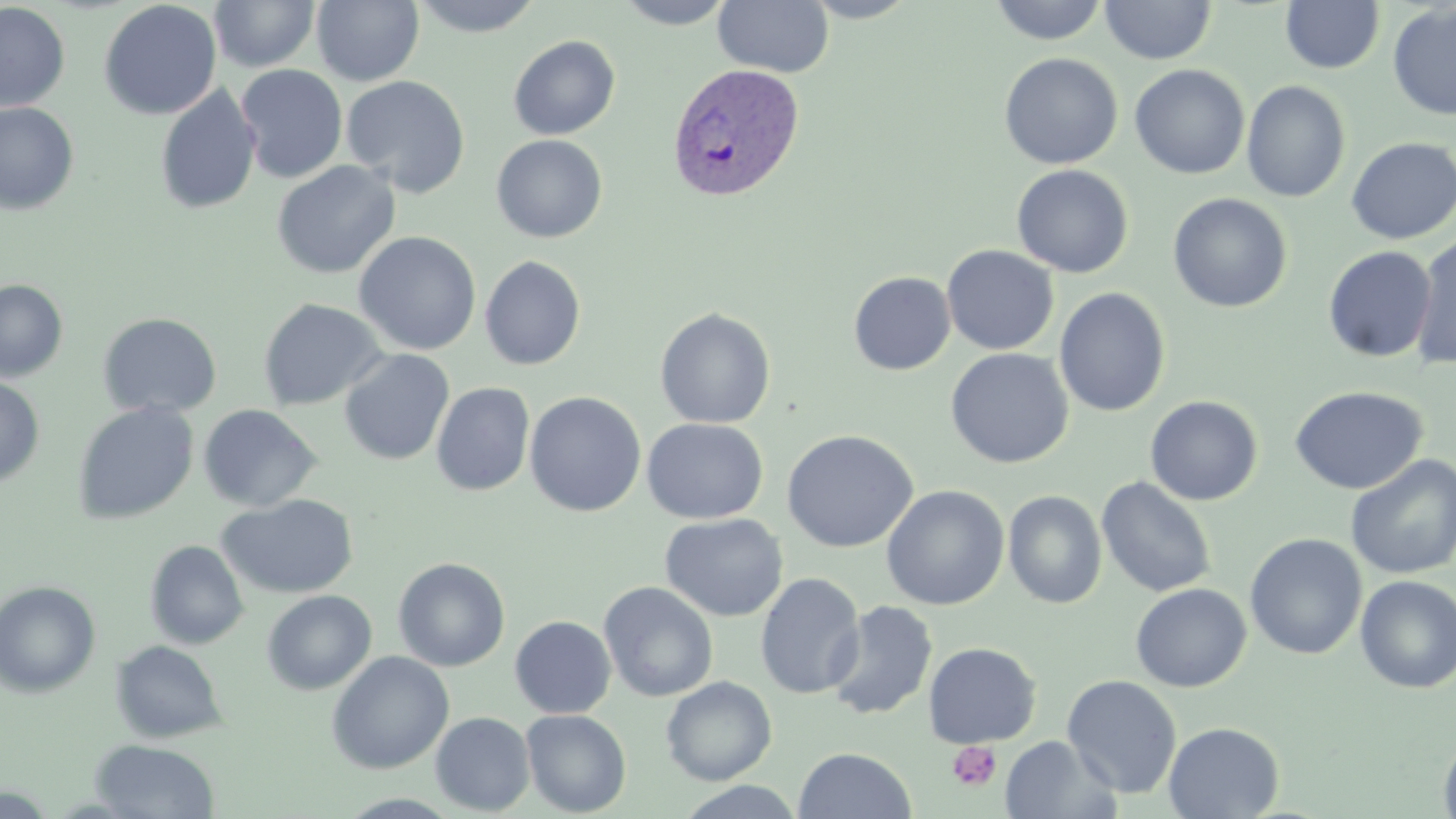

slide-level diagnosis = Plasmodium vivax
magnification = 1000x
Plasmodium vivax-infected red blood cell locations = approximate bounding boxes as [x1, y1, x2, y2] in pixels: [667, 62, 804, 202]
image size = 1456×819 pixels
uninfected red blood cell locations = approximate bounding boxes as [x1, y1, x2, y2] in pixels: [209, 0, 320, 72], [311, 0, 424, 86], [408, 0, 545, 37], [614, 0, 736, 29], [713, 0, 835, 78], [798, 0, 922, 23], [989, 0, 1110, 45], [99, 1, 222, 120], [1099, 1, 1217, 65], [1281, 1, 1384, 74], [0, 2, 70, 113], [1387, 3, 1456, 120], [508, 35, 620, 140], [999, 52, 1123, 170], [235, 64, 348, 183], [1130, 64, 1250, 179], [341, 75, 471, 197], [1241, 80, 1351, 203], [154, 82, 261, 215], [0, 101, 79, 215], [491, 134, 608, 243], [1345, 136, 1456, 245], [271, 160, 400, 279], [1011, 164, 1134, 278], [1168, 193, 1293, 313], [354, 231, 481, 355], [1410, 231, 1456, 371], [941, 244, 1059, 355], [1323, 245, 1437, 363], [479, 256, 586, 371], [848, 271, 955, 376], [0, 279, 68, 382], [1054, 287, 1171, 417], [258, 297, 388, 411], [654, 307, 776, 429], [97, 312, 222, 419], [945, 348, 1073, 469], [338, 349, 455, 466], [0, 375, 45, 489], [431, 382, 535, 497], [1290, 386, 1428, 495], [524, 391, 647, 517], [1145, 395, 1263, 506], [72, 402, 200, 525], [197, 404, 322, 512], [642, 418, 768, 524], [781, 429, 919, 553], [1344, 453, 1456, 580], [1096, 477, 1216, 598], [881, 485, 1009, 610], [1003, 490, 1107, 609], [217, 494, 359, 599], [659, 513, 789, 623], [1245, 533, 1367, 660], [145, 540, 249, 649], [392, 557, 511, 672], [754, 571, 866, 700], [1355, 574, 1456, 694], [0, 580, 102, 698], [598, 581, 719, 702], [1129, 583, 1252, 692], [262, 590, 377, 695], [824, 600, 938, 721], [509, 615, 616, 718], [110, 640, 228, 743], [923, 642, 1042, 748], [326, 651, 454, 774], [1063, 674, 1182, 798], [661, 676, 777, 785], [521, 709, 631, 817], [430, 711, 535, 816], [1163, 721, 1284, 818], [1438, 732, 1456, 819], [999, 734, 1121, 819], [90, 738, 220, 819], [793, 747, 916, 818], [671, 781, 808, 819]
preparation = thin blood film
modality = light microscopy
stain = May-Grünwald-Giemsa
field of view = one of a larger specimen
platelet locations = approximate bounding boxes as [x1, y1, x2, y2] in pixels: [946, 741, 1003, 792]